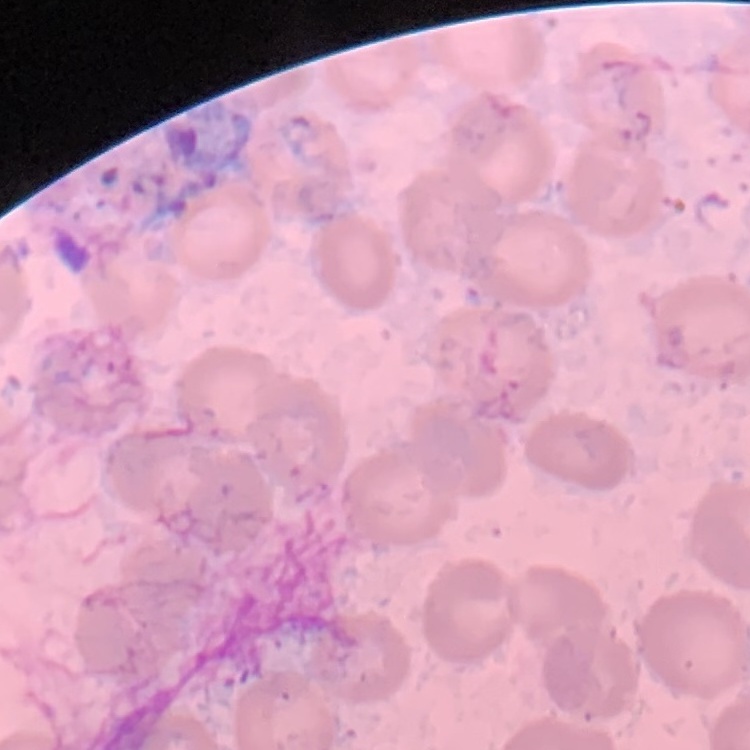

The erythrocytes exhibit no rouleaux formation. Field's or Giemsa stain. One tile cut from a larger photomicrograph. Thin blood smear.